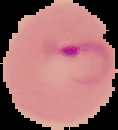
image size = 118×130 pixels
image type = cell region segmented out of the field of view; surrounding area masked to black
preparation = thin blood smear
result = Plasmodium parasites detected